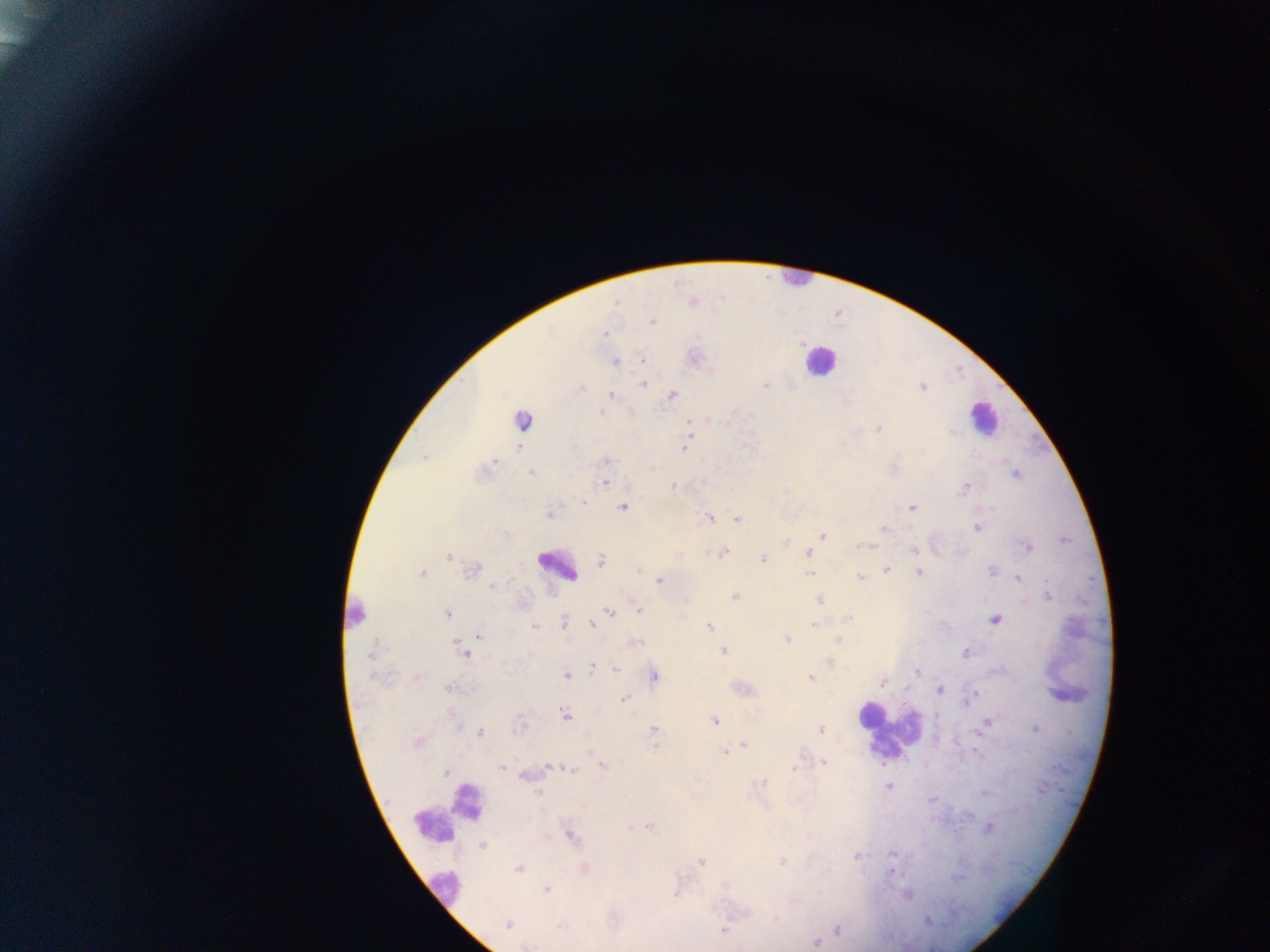
country: Ghana
capture: mobile-phone photograph through a microscope
image_size: 1270×952 pixels
field_of_view: single
plasmodium_parasite_locations: 'approximate centers as x y in pixels: 617 302; 652 321; 605 334; 643 359; 615 362; 644 384; 765 385; 923 387; 582 388; 672 394; 611 395; 601 412; 522 420; 689 421; 879 428; 519 447; 685 449; 425 457; 494 461; 606 461; 531 474; 1016 474; 605 482; 965 486; 673 487; 583 502; 622 507; 912 508; 550 515; 709 518; 737 519; 977 527; 884 529; 823 535; 862 546; 1029 548; 914 549; 724 553; 808 553; 448 556; 763 558; 601 561; 472 569; 886 570; 638 571; 422 572; 919 572; 991 572; 810 574; 860 576; 1019 578; 659 580; 492 586; 734 596; 1048 596; 820 600; 638 609; 610 612; 448 613; 849 617; 997 619; 596 620; 564 622; 592 623; 814 625; 534 626; 709 627; 480 636; 786 639; 839 641; 635 643; 723 651; 966 652; 464 653; 370 656; 591 667; 616 668; 917 672; 566 675; 654 676; 811 678; 883 683; 449 688; 939 690; 973 695; 623 699; 967 701; 565 715; 715 721; 987 723; 1035 729; 654 730; 821 731; 480 732; 417 742; 744 745; 724 752; 824 762; 603 765; 550 767; 502 768; 794 768; 572 770; 446 772; 888 786; 537 793; 986 793; 932 799; 650 827; 989 828; 572 836; 482 846; 893 854; 856 856; 782 861; 701 862; 519 869; 585 869; 892 871; 547 889; 675 895; 907 896; 776 919; 927 921; 508 923; 558 926; 723 930; 838 930; 815 942; 525 946'
preparation: thick blood smear
leukocyte_locations: 'approximate centers as x y in pixels: 794 279; 820 361; 983 418; 558 566; 888 732; 446 813; 446 889'